Give the extent of all Trypanosoma brucei.
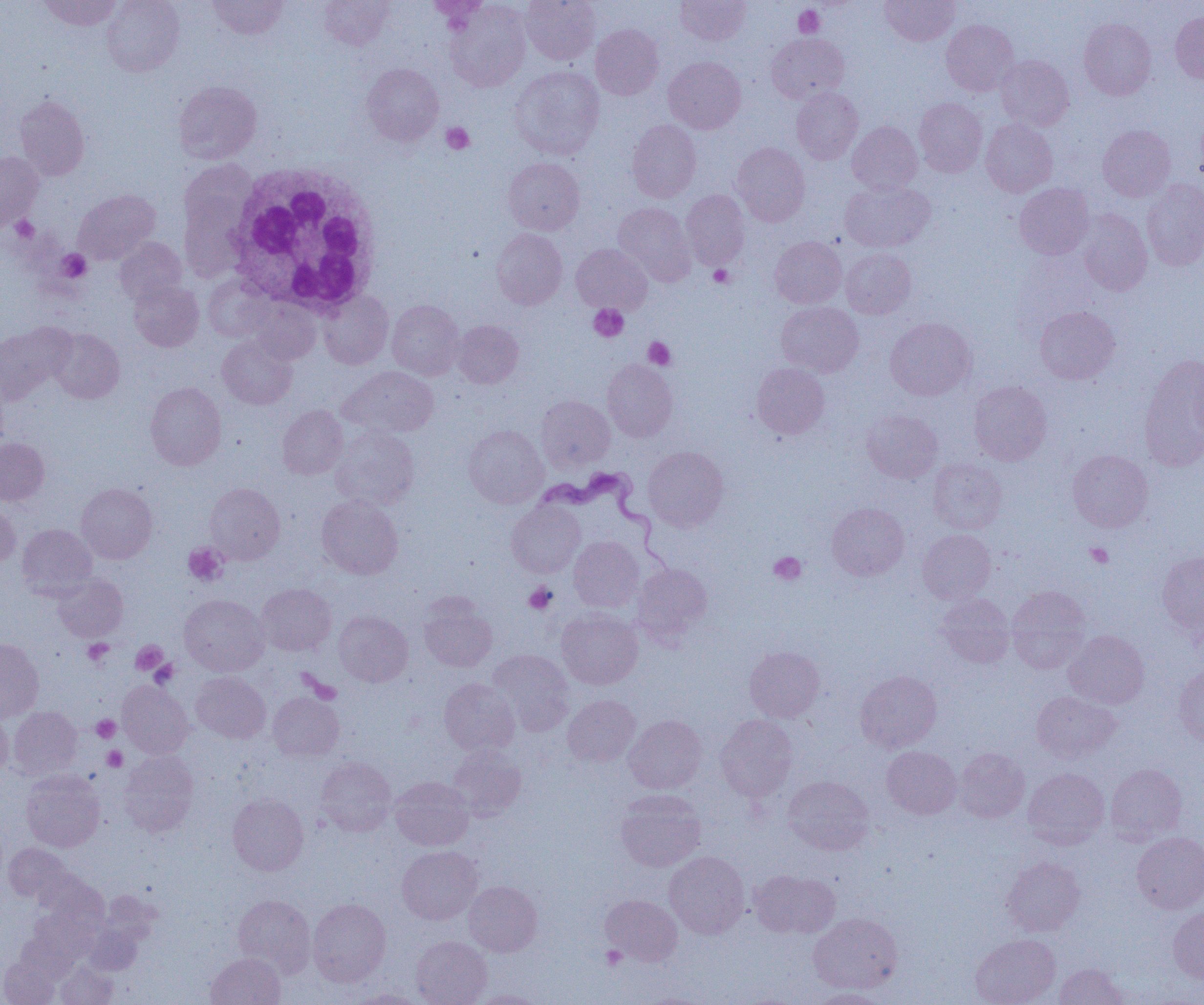

Approximate bounding boxes as (x1, y1, x2, y2) in pixels.
Trypanosoma brucei: (532, 468, 668, 568).

Uninfected red blood cell locations: (38, 0, 122, 31), (101, 0, 184, 76), (207, 0, 289, 39), (425, 0, 491, 22), (521, 0, 600, 65), (676, 0, 750, 45), (880, 0, 960, 46), (319, 1, 393, 50), (445, 1, 531, 92), (1170, 11, 1204, 83), (1079, 18, 1156, 99), (941, 20, 1019, 96), (590, 24, 663, 100), (766, 33, 849, 103), (996, 55, 1074, 131), (663, 56, 746, 134), (362, 63, 444, 146), (509, 66, 604, 159), (173, 81, 262, 163), (791, 87, 863, 164), (14, 95, 89, 180), (914, 97, 987, 176), (1194, 110, 1204, 188), (627, 119, 701, 203), (981, 119, 1057, 197), (847, 121, 922, 195), (1098, 125, 1175, 201), (731, 143, 810, 226), (0, 151, 43, 231), (503, 157, 585, 235), (179, 159, 258, 237), (1141, 179, 1204, 270), (840, 180, 934, 252), (1015, 183, 1094, 259), (73, 189, 160, 264), (179, 189, 250, 283), (681, 190, 749, 269), (613, 202, 695, 285), (1077, 209, 1152, 295), (492, 229, 567, 309), (770, 236, 846, 308), (114, 237, 186, 304), (571, 244, 653, 314), (840, 248, 916, 318), (204, 276, 273, 343), (129, 280, 203, 352), (317, 290, 393, 369), (247, 298, 321, 363), (387, 300, 464, 379), (776, 302, 863, 377), (1035, 306, 1120, 384), (885, 317, 976, 400), (452, 320, 523, 388), (0, 321, 76, 403), (47, 328, 124, 403), (217, 334, 297, 409), (1139, 354, 1204, 471), (602, 359, 677, 441), (752, 363, 830, 439), (340, 366, 439, 438), (0, 377, 9, 454), (969, 381, 1051, 465), (145, 382, 226, 470), (536, 395, 615, 471), (277, 405, 348, 479), (862, 409, 942, 483), (464, 425, 548, 508), (329, 426, 419, 510), (0, 438, 49, 505), (643, 446, 728, 531), (1068, 449, 1153, 532), (928, 458, 1007, 534), (76, 483, 157, 563), (205, 483, 285, 564), (316, 495, 403, 579), (0, 501, 20, 566), (507, 501, 585, 577), (827, 503, 909, 580), (17, 523, 97, 600), (917, 529, 996, 604), (569, 536, 644, 612), (1157, 551, 1204, 636), (632, 562, 713, 645), (53, 574, 128, 642), (256, 583, 336, 655), (1007, 586, 1091, 673), (936, 593, 1014, 667), (179, 594, 269, 676), (419, 597, 497, 672), (556, 609, 643, 689), (334, 610, 413, 686), (1064, 630, 1149, 708), (0, 639, 43, 721), (744, 646, 825, 722), (487, 649, 574, 735), (1174, 665, 1204, 745), (855, 670, 941, 752), (191, 672, 270, 743), (439, 678, 520, 756), (117, 680, 193, 759), (1032, 690, 1120, 763), (268, 691, 344, 761), (562, 695, 640, 767), (9, 706, 81, 777), (0, 710, 12, 777), (624, 715, 707, 794), (716, 715, 798, 801), (447, 744, 527, 820), (882, 746, 961, 819), (953, 748, 1029, 823), (118, 752, 198, 837), (315, 757, 397, 836), (1105, 763, 1187, 843), (1023, 768, 1109, 849), (21, 770, 105, 852), (783, 775, 874, 855), (390, 776, 473, 850), (615, 789, 706, 872), (228, 794, 309, 875), (1132, 832, 1204, 913), (4, 844, 73, 904), (397, 846, 483, 924), (664, 851, 750, 938), (1001, 856, 1085, 936), (39, 869, 108, 929), (749, 869, 841, 937), (464, 880, 542, 956), (600, 894, 683, 966), (233, 895, 315, 975), (308, 898, 391, 986), (1168, 907, 1204, 982), (808, 912, 902, 994), (970, 934, 1060, 1005), (411, 935, 492, 1005), (206, 952, 286, 1005), (1, 956, 59, 1005), (55, 961, 117, 1004), (1054, 963, 1128, 1005), (350, 988, 428, 1005), (807, 988, 893, 1004), (468, 989, 548, 1005). Platelet locations: (794, 5, 825, 37), (441, 122, 474, 154), (10, 216, 39, 243), (57, 249, 91, 282), (709, 264, 733, 287), (589, 304, 628, 341), (643, 337, 676, 370), (183, 543, 228, 586), (1086, 543, 1113, 568), (769, 552, 806, 585), (524, 582, 557, 614), (83, 639, 113, 666), (131, 641, 168, 674), (149, 660, 177, 686), (91, 715, 121, 742), (102, 746, 127, 770), (601, 945, 627, 968). White blood cell locations: (225, 161, 384, 314). Slide-level diagnosis: Trypanosoma brucei. Thin blood film. Single field of view. Optical microscopy. Image is 1204×1005 pixels. Captured at 1000x magnification.